State which cell type is depicted.
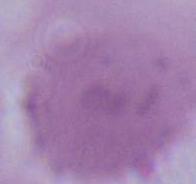
An erythrocyte.

modality = photomicrograph
magnification = 1000x